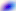

Summary:
  - Identification: Toxoplasma gondii
  - Modality: micrograph
  - Magnification: 400x